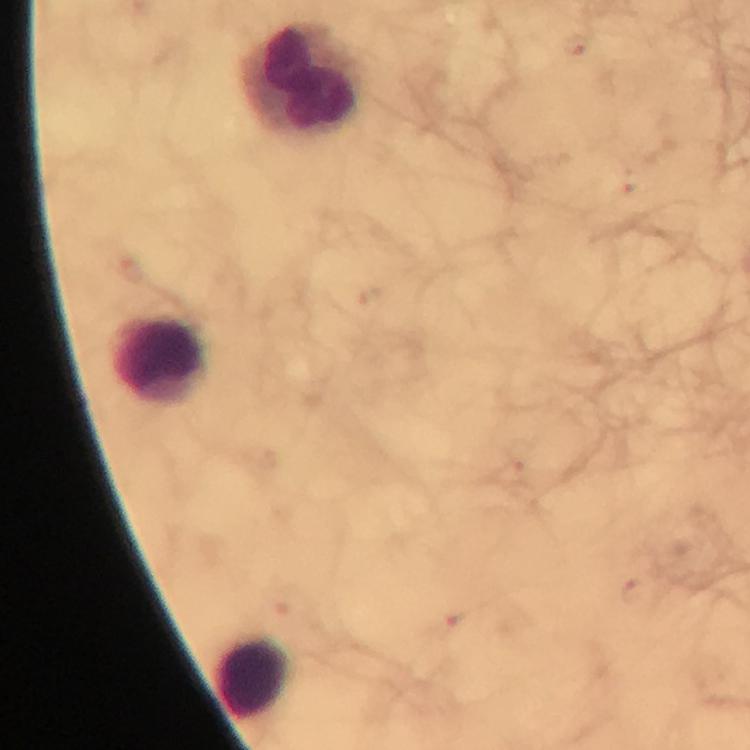 Approximate centers as (x, y) in pixels. Leukocyte locations: (302, 79), (160, 361), (253, 678). Image is 750×750 pixels. From a diagnostic examination for malaria. Giemsa-stained preparation. Plasmodium parasites: none detected. Thick blood film. Immersion oil applied. 100x magnification. Photographed with a smartphone mounted on the microscope. A crop from one field of view.